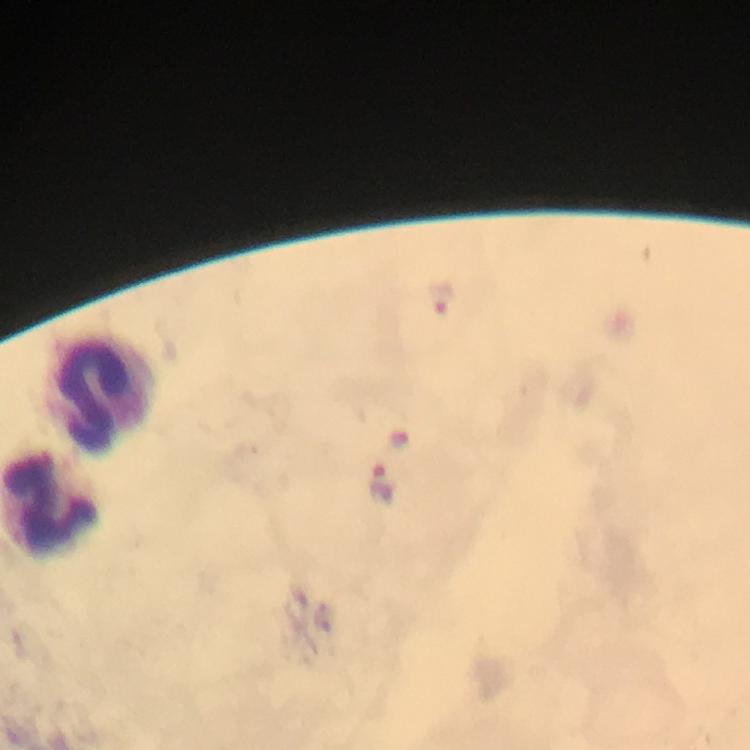

Approximate centers as [x, y] in pixels. Malaria parasite locations: [440, 297], [379, 481]. Leukocyte locations: [95, 398], [50, 508]. At 100x magnification. Giemsa-stained preparation. Smartphone photograph taken through a microscope. Thick blood smear. Image is 750×750 pixels. Immersion oil applied. Cropped region of a single field of view. From a malaria diagnostic workup.